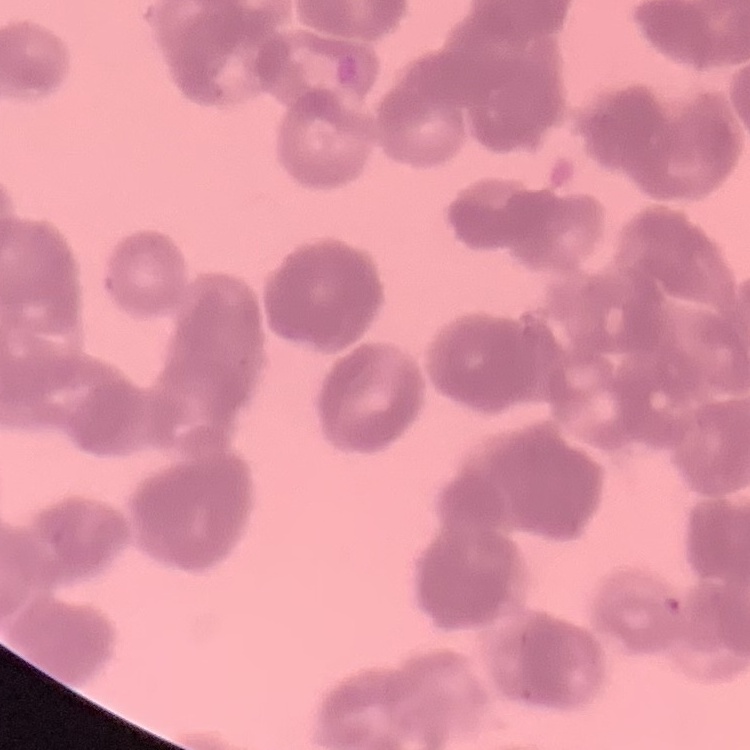

{
  "erythrocyte_morphology": "rouleaux formation",
  "image_type": "one tile cut from a larger photomicrograph",
  "preparation": "thin blood smear",
  "stain": "Field's or Giemsa"
}